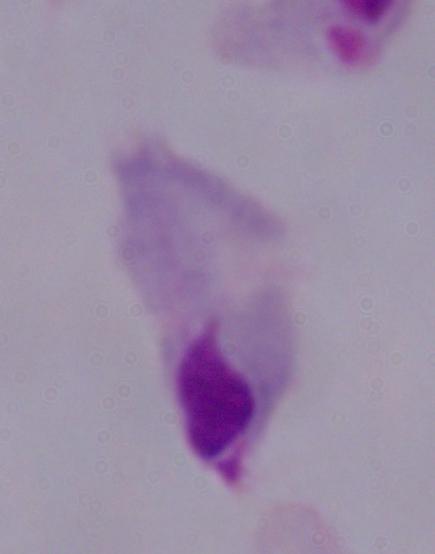
Summary:
  - Modality: micrograph
  - Magnification: 1000x
  - Identification: trichomonad